Report the malaria status of this cell.
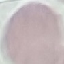
It is uninfected.

Summary:
  - Image type: cell patch, automatically extracted from a larger field of view and resized to 64 × 64 pixels
  - Stain: Giemsa
  - Preparation: thin blood film
  - Capture: smartphone through the microscope eyepiece